Name the parasite shown.
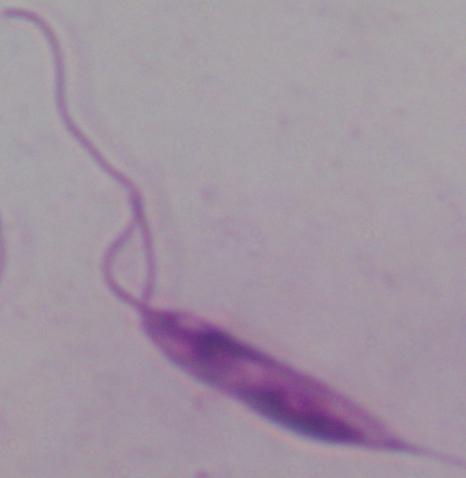

Leishmania.

modality = photomicrograph
magnification = 1000x